Outline each uninfected red blood cell.
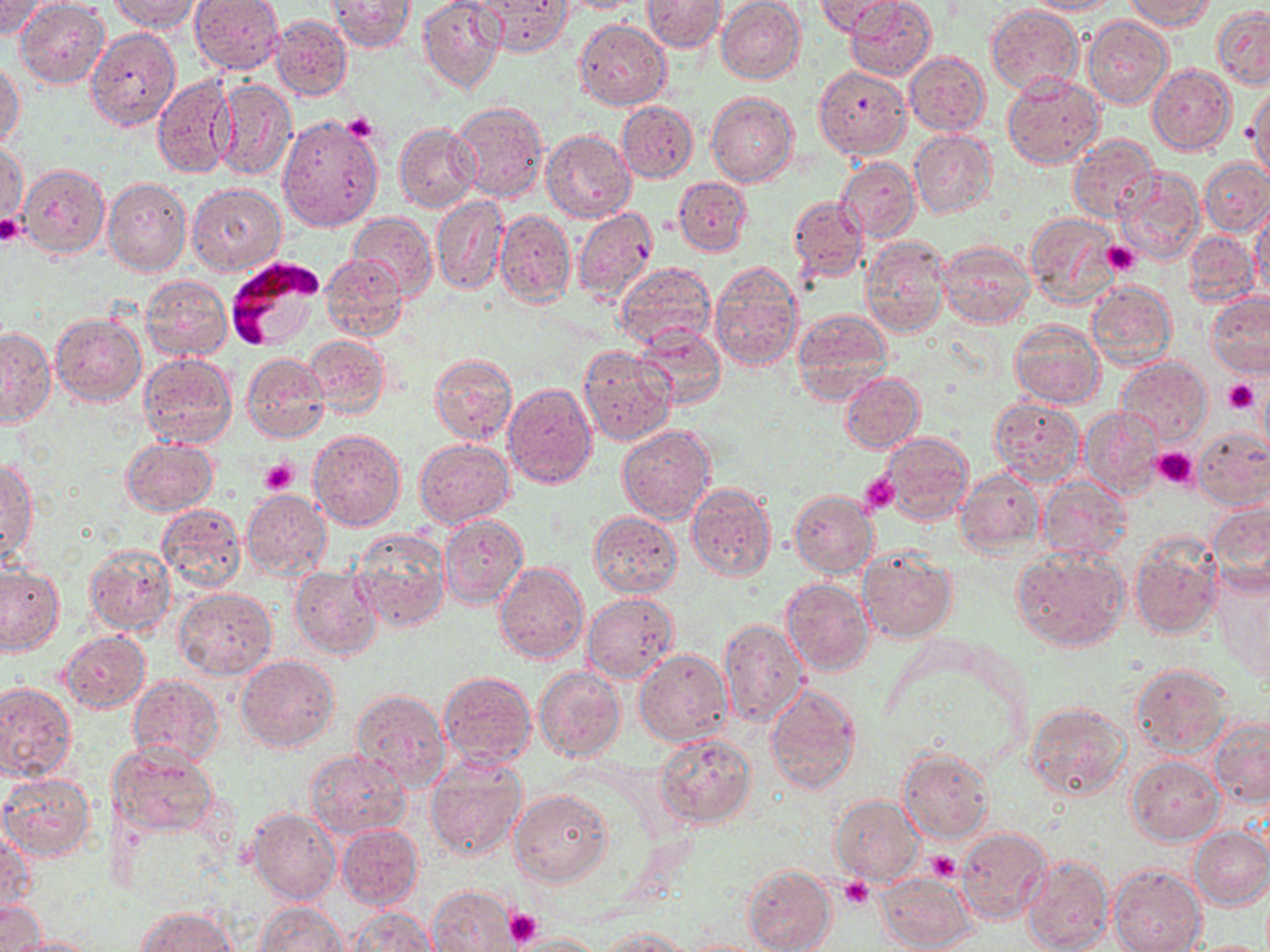

Approximate bounding boxes as (x1,y1)-(x2,y2) corner pairs in pixels.
Uninfected red blood cells: (1,0)-(52,41), (14,0)-(109,88), (110,0)-(201,33), (189,0)-(284,74), (418,0)-(504,93), (555,0)-(643,13), (643,0)-(726,53), (814,0)-(902,38), (845,0)-(936,79), (1023,0)-(1119,16), (1123,0)-(1214,29), (328,1)-(415,52), (469,1)-(570,56), (716,1)-(805,84), (986,4)-(1083,95), (1213,7)-(1270,89), (270,16)-(352,100), (1083,16)-(1172,108), (576,20)-(671,111), (85,27)-(181,130), (904,50)-(991,136), (1,61)-(23,148), (1148,64)-(1236,156), (814,66)-(910,158), (152,74)-(237,179), (1003,74)-(1104,167), (212,79)-(297,181), (1246,85)-(1269,181), (707,90)-(798,187), (616,100)-(697,183), (450,101)-(548,203), (277,115)-(383,230), (395,123)-(480,212), (542,130)-(635,222), (909,130)-(998,219), (1069,135)-(1159,222), (1,141)-(27,230), (837,157)-(919,241), (1198,159)-(1269,236), (17,162)-(109,259), (1115,166)-(1206,266), (674,176)-(753,257), (103,178)-(191,277), (188,183)-(285,276), (432,196)-(509,294), (789,196)-(867,282), (1251,203)-(1270,300), (572,208)-(659,303), (494,209)-(575,308), (1025,212)-(1122,309), (348,213)-(436,297), (1185,230)-(1259,307), (861,235)-(951,336), (937,241)-(1036,328), (321,252)-(408,342), (707,260)-(803,372), (613,261)-(716,353), (140,275)-(232,360), (1087,281)-(1177,371), (1206,293)-(1270,378), (791,308)-(893,401), (50,312)-(146,407), (1010,317)-(1104,408), (1000,323)-(1092,483), (0,325)-(55,428), (633,327)-(724,410), (304,335)-(389,419), (578,344)-(675,445), (136,352)-(237,450), (242,352)-(329,442), (428,354)-(517,445), (1117,356)-(1211,445), (841,373)-(924,454), (1257,382)-(1270,457), (502,383)-(597,488), (989,398)-(1084,485), (1079,407)-(1165,500), (617,425)-(716,524), (1193,427)-(1270,509), (308,430)-(406,532), (881,432)-(975,525), (120,438)-(217,516), (415,439)-(514,528), (0,459)-(37,566), (956,468)-(1045,555), (1039,477)-(1130,564), (686,481)-(777,582), (242,489)-(331,580), (789,490)-(878,578), (1205,500)-(1270,595), (156,502)-(246,594), (588,511)-(682,597), (440,512)-(527,607), (350,530)-(449,631), (1129,533)-(1221,640), (84,544)-(177,636), (858,546)-(959,644), (1013,549)-(1129,650), (0,561)-(66,657), (495,562)-(589,664), (1212,564)-(1270,679), (290,566)-(383,659), (781,578)-(876,675), (173,588)-(277,680), (583,594)-(678,682), (718,617)-(809,728), (60,630)-(150,713), (634,650)-(733,746), (236,655)-(340,753), (1130,663)-(1233,754), (534,668)-(624,761), (438,671)-(537,769), (128,675)-(224,765), (1,681)-(76,780), (765,685)-(862,794), (351,688)-(448,791), (1023,702)-(1131,802), (1206,715)-(1270,808), (655,735)-(756,829), (109,743)-(218,836), (898,747)-(994,844), (304,749)-(411,837), (425,755)-(527,861), (1127,755)-(1225,845), (0,772)-(97,862), (510,788)-(612,886), (832,795)-(925,884), (247,807)-(340,906), (336,824)-(423,913), (1189,826)-(1270,910), (957,827)-(1053,925), (0,829)-(34,924), (1022,853)-(1114,952), (742,864)-(836,952), (1109,864)-(1206,952), (874,871)-(976,951), (428,886)-(518,951), (0,900)-(44,951), (253,901)-(353,951), (135,906)-(237,952), (345,907)-(437,950), (597,925)-(693,951), (513,932)-(604,952), (5,936)-(103,952), (683,937)-(769,952).

slide-level diagnosis = Plasmodium falciparum
field of view = one of a larger specimen
modality = optical microscopy
platelet locations = approximate bounding boxes as (x1,y1)-(x2,y2) corner pairs in pixels: (342,113)-(380,144), (0,219)-(24,246), (1103,241)-(1141,276), (1223,378)-(1259,415), (1151,446)-(1197,489), (260,458)-(297,495), (858,472)-(900,515), (926,852)-(961,883), (839,877)-(874,910), (503,909)-(542,948)
magnification = 1000x
Plasmodium falciparum-infected red blood cell locations = approximate bounding boxes as (x1,y1)-(x2,y2) corner pairs in pixels: (225,257)-(324,351)
stain = May-Grünwald-Giemsa
preparation = thin blood smear
image size = 1270×952 pixels